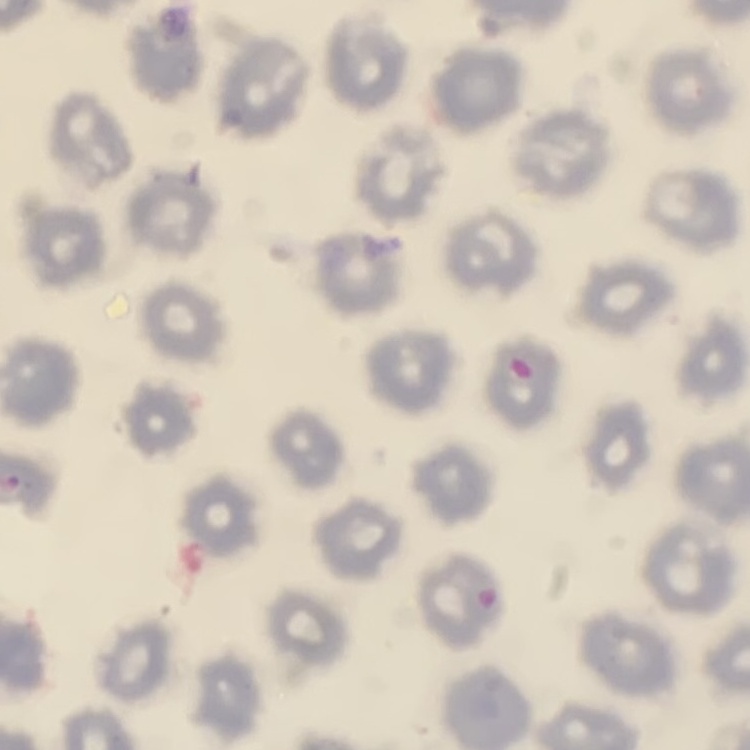
{
  "red_blood_cell_morphology": "no rouleaux formation",
  "preparation": "thin blood film",
  "image_type": "square crop of a larger photomicrograph",
  "stain": "Field's or Giemsa"
}